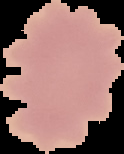

{
  "preparation": "thin blood film",
  "image_type": "segmented cell region with the area outside set to black",
  "result": "negative for Plasmodium parasites",
  "image_size": "124×154 pixels"
}